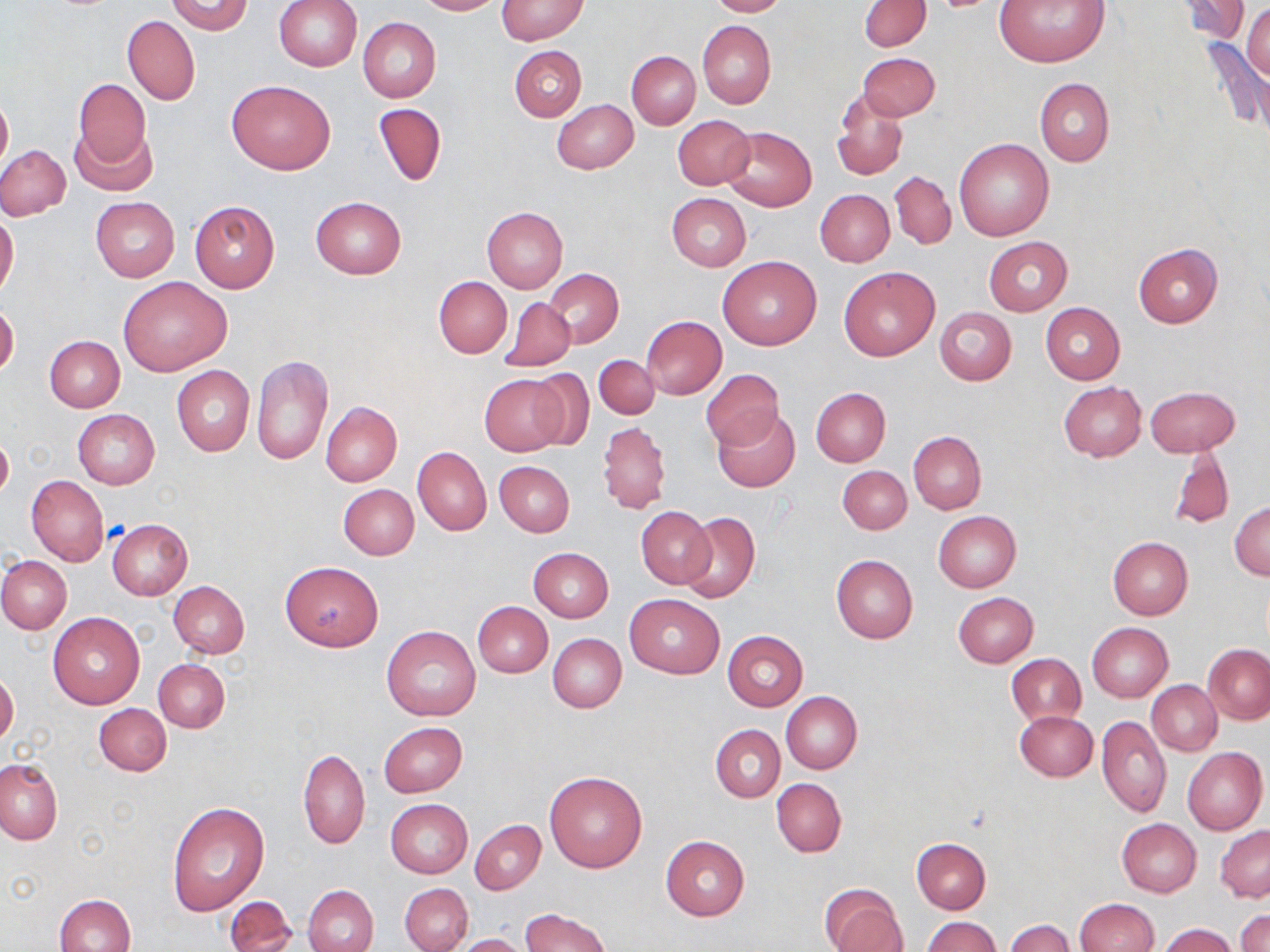 Approximate bounding boxes as (x1, y1, x2, y2) in pixels. Uninfected red blood cell locations: (414, 0, 499, 15), (707, 0, 790, 17), (859, 0, 931, 51), (993, 0, 1111, 68), (1177, 0, 1251, 44), (164, 1, 253, 35), (274, 1, 361, 71), (497, 1, 589, 43), (1243, 4, 1269, 82), (123, 17, 200, 104), (358, 17, 441, 102), (698, 20, 775, 110), (1203, 40, 1269, 132), (510, 45, 586, 121), (626, 51, 700, 128), (857, 53, 940, 121), (73, 78, 151, 174), (1034, 78, 1114, 166), (227, 80, 335, 175), (832, 91, 909, 181), (0, 92, 12, 172), (552, 99, 638, 174), (374, 103, 446, 186), (672, 114, 756, 190), (69, 122, 156, 196), (721, 126, 817, 212), (954, 138, 1054, 242), (0, 146, 71, 220), (891, 170, 956, 249), (815, 189, 894, 267), (666, 193, 751, 271), (91, 197, 179, 282), (310, 197, 407, 279), (189, 201, 279, 293), (482, 207, 569, 293), (0, 212, 19, 297), (984, 237, 1072, 316), (1133, 243, 1222, 327), (718, 255, 822, 350), (838, 266, 939, 361), (545, 268, 623, 348), (120, 276, 231, 374), (433, 276, 511, 358), (500, 298, 576, 371), (1040, 303, 1125, 383), (0, 304, 19, 377), (935, 307, 1016, 384), (641, 315, 727, 398), (43, 335, 125, 412), (594, 353, 660, 419), (251, 355, 333, 465), (171, 366, 255, 455), (701, 369, 784, 452), (526, 370, 596, 450), (479, 373, 568, 455), (1058, 381, 1147, 461), (1145, 386, 1240, 457), (812, 387, 890, 467), (321, 402, 402, 486), (712, 408, 801, 493), (73, 409, 159, 488), (597, 421, 670, 514), (908, 431, 986, 513), (1, 433, 13, 502), (1166, 446, 1234, 532), (413, 447, 492, 536), (494, 461, 575, 537), (837, 465, 911, 534), (27, 476, 108, 565), (339, 484, 419, 559), (1230, 501, 1270, 580), (637, 505, 716, 588), (934, 511, 1020, 592), (679, 512, 760, 604), (107, 519, 192, 600), (1107, 535, 1194, 620), (529, 548, 613, 622), (831, 554, 918, 643), (0, 555, 73, 634), (282, 561, 383, 651), (170, 581, 250, 658), (954, 592, 1037, 667), (624, 594, 725, 679), (473, 601, 551, 677), (48, 613, 145, 708), (1088, 623, 1173, 702), (382, 625, 480, 721), (723, 631, 807, 711), (547, 633, 626, 712), (1204, 644, 1270, 724), (1006, 654, 1086, 727), (154, 659, 229, 732), (0, 672, 20, 746), (1148, 681, 1222, 756), (781, 691, 862, 774), (94, 703, 171, 776), (1014, 709, 1098, 782), (1097, 715, 1171, 818), (379, 721, 467, 797), (711, 724, 785, 801), (1182, 746, 1267, 834), (298, 748, 370, 849), (0, 758, 63, 844), (545, 771, 648, 873), (772, 778, 846, 857), (386, 799, 473, 878), (167, 801, 269, 916), (1117, 818, 1202, 896), (469, 819, 545, 894), (1215, 824, 1270, 902), (661, 835, 749, 921), (911, 839, 990, 914), (400, 883, 473, 952), (304, 884, 378, 952), (820, 884, 906, 951), (229, 892, 374, 949), (54, 893, 135, 952), (225, 896, 297, 951), (1074, 898, 1159, 951), (519, 909, 612, 952), (1236, 910, 1270, 952), (921, 916, 1000, 952), (1005, 919, 1074, 951), (1158, 923, 1238, 952), (455, 933, 529, 952). Slide-level diagnosis: no evidence of blood parasites. Optical microscopy. Single field of view. Thin blood film. 1000x magnification. Image is 1270×952 pixels. May-Grünwald-Giemsa-stained preparation.